Identify the preparation type.
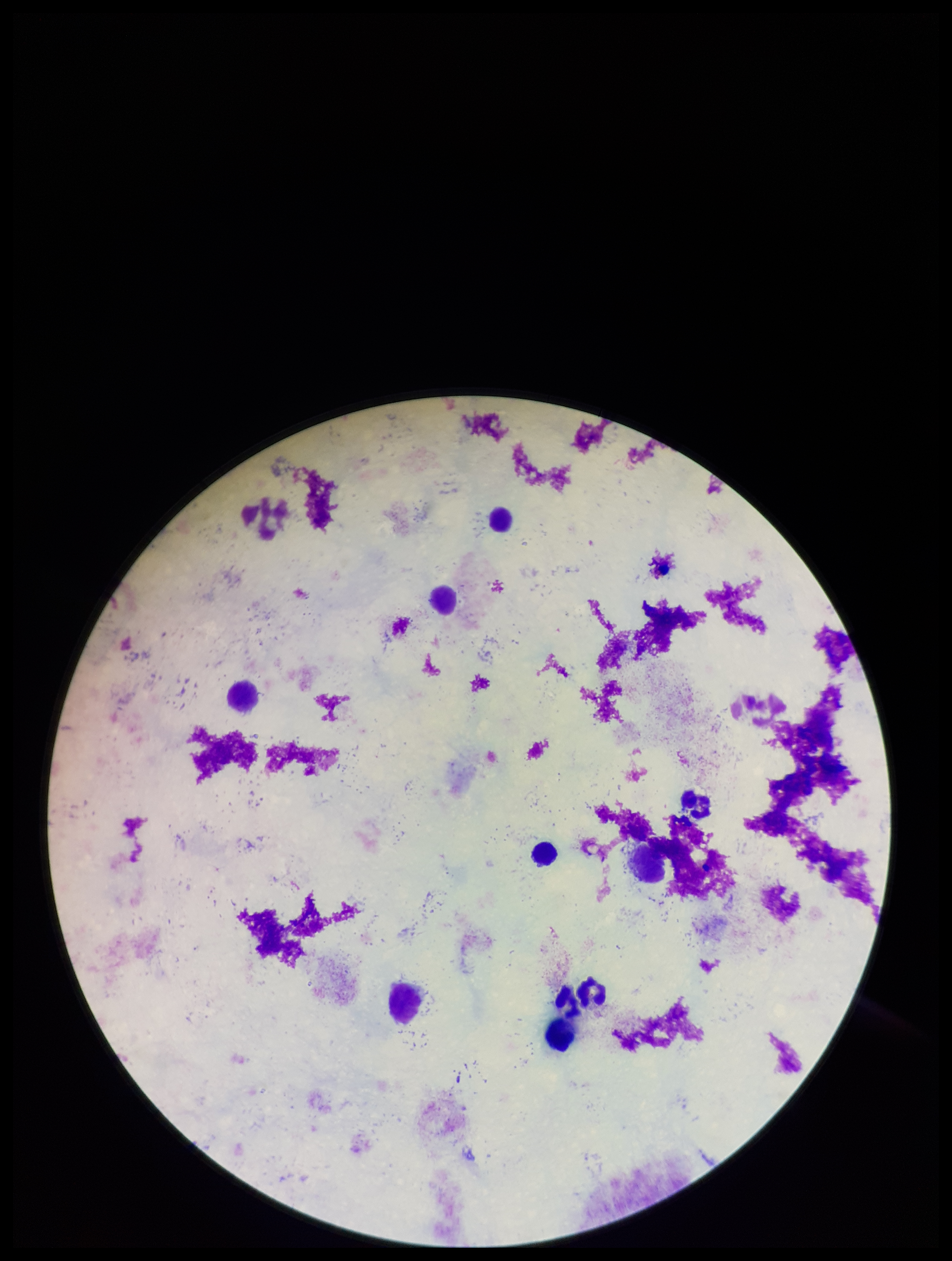

It is a thick blood smear.

{
  "capture": "smartphone photograph through the microscope eyepiece",
  "image_size": "952×1261 pixels",
  "patient_malaria_status": "negative",
  "parasite_count": 0,
  "stain": "Giemsa",
  "plasmodium_parasites": "none identified",
  "field_of_view": "one from this slide",
  "leukocyte_count": 8
}